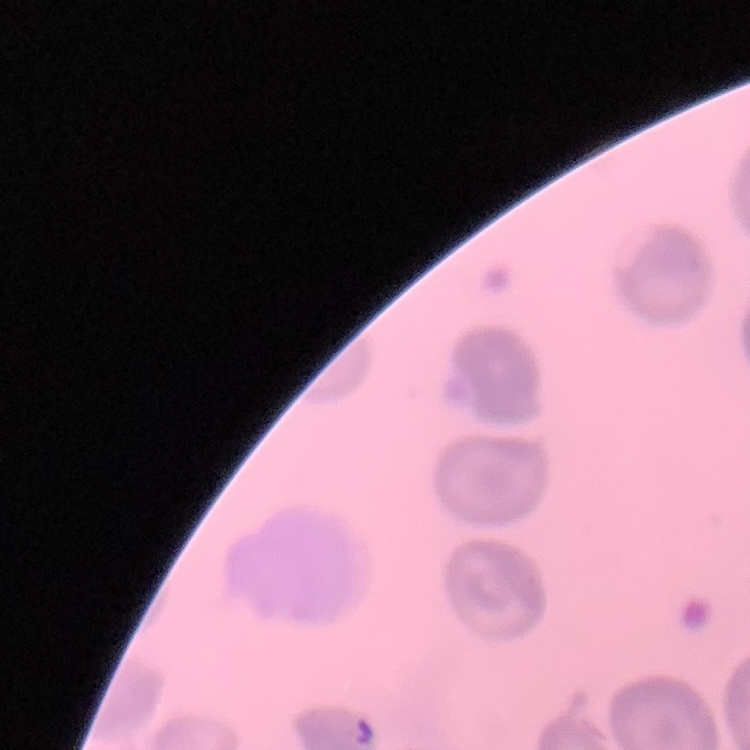
Summary:
  - Red blood cell morphology: no rouleaux formation
  - Preparation: thin peripheral smear
  - Image type: square crop of a larger photomicrograph
  - Stain: Field's or Giemsa